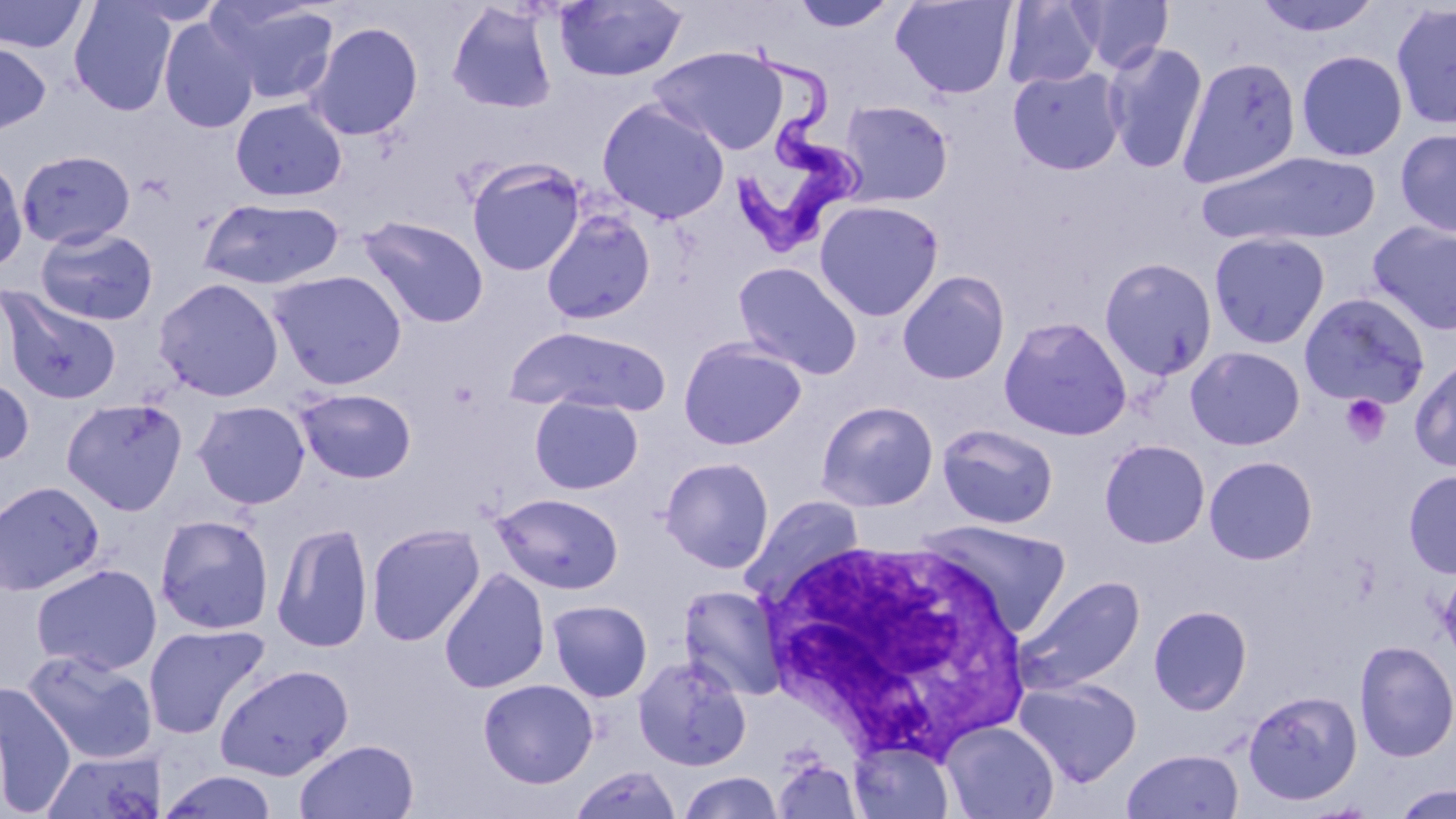

Summary:
  - Coordinate format: approximate bounding boxes as (x1,y1)-(x2,y2) corner pairs in pixels
  - Platelet locations: (1339,394)-(1391,447)
  - Trypanosoma brucei locations: (721,37)-(869,257)
  - Uninfected red blood cell locations: (0,0)-(89,54), (68,0)-(178,116), (554,0)-(688,82), (790,0)-(898,33), (890,0)-(1017,99), (1073,0)-(1173,73), (1252,0)-(1384,38), (208,1)-(341,105), (1002,1)-(1102,89), (446,2)-(559,115), (1390,2)-(1456,131), (158,17)-(260,133), (306,21)-(424,142), (0,40)-(52,136), (1102,41)-(1209,175), (650,46)-(788,155), (1296,50)-(1408,162), (1177,56)-(1302,188), (1007,66)-(1127,176), (596,98)-(730,224), (230,99)-(347,202), (837,99)-(954,206), (1395,128)-(1456,238), (16,149)-(136,250), (1196,151)-(1381,247), (0,157)-(28,274), (466,159)-(586,276), (198,197)-(344,290), (813,199)-(944,321), (541,210)-(657,325), (357,215)-(489,328), (1366,221)-(1456,335), (34,226)-(159,325), (1209,232)-(1331,349), (1099,257)-(1218,381), (732,261)-(863,379), (268,269)-(408,389), (897,270)-(1011,385), (153,277)-(285,401), (0,287)-(122,405), (1298,292)-(1431,410), (998,315)-(1132,441), (505,325)-(670,416), (678,337)-(807,450), (1185,345)-(1306,451), (1409,354)-(1456,472), (0,373)-(34,467), (294,388)-(417,484), (530,395)-(644,494), (61,397)-(188,515), (816,400)-(939,511), (192,401)-(311,509), (937,423)-(1059,529), (1099,439)-(1210,549), (1204,455)-(1318,565), (659,457)-(775,573), (1403,469)-(1456,579), (0,479)-(105,596), (492,492)-(624,594), (741,494)-(865,602), (154,513)-(275,635), (918,519)-(1071,637), (271,521)-(374,653), (366,523)-(485,646), (30,563)-(162,676), (1437,564)-(1456,670), (439,568)-(550,694), (1013,575)-(1145,696), (678,585)-(787,700), (547,599)-(652,701), (1148,605)-(1253,715), (143,622)-(270,740), (1354,641)-(1456,761), (22,649)-(158,765), (633,655)-(752,771), (214,663)-(354,780), (1014,677)-(1141,786), (478,679)-(599,788), (0,681)-(77,818), (1242,689)-(1363,806), (939,721)-(1060,819), (294,739)-(419,819), (850,741)-(955,819), (41,749)-(164,818), (1122,749)-(1244,818), (771,758)-(863,819), (569,764)-(683,819), (157,771)-(279,818), (678,772)-(783,818), (1392,784)-(1456,819)
  - White blood cell locations: (749,535)-(1033,764)
  - Slide-level diagnosis: Trypanosoma brucei
  - Preparation: thin blood film
  - Image size: 1456×819 pixels
  - Field of view: one of a larger specimen
  - Stain: May-Grünwald-Giemsa
  - Modality: optical microscopy
  - Magnification: 1000x